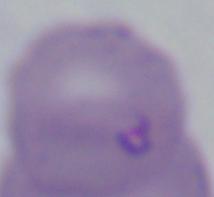

Summary:
  - Identification: Babesia
  - Modality: micrograph
  - Magnification: 1000x